Identify the parasite.
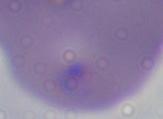

Babesia.

1000x magnification. Photomicrograph.